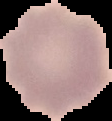 From a thin blood smear. Result: no malaria parasites detected. Image is 112×121 pixels. Segmented cell region on a black background.